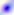 Micrograph. 400x magnification. Toxoplasma gondii is shown.